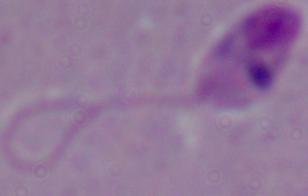

A Leishmania parasite is shown. Photomicrograph. 1000x magnification.